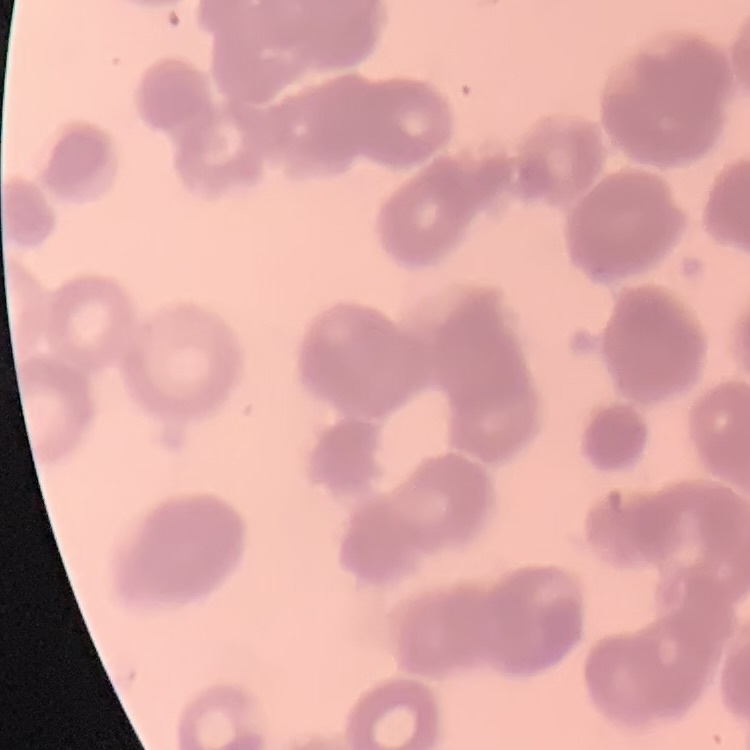

Summary:
  - Erythrocyte morphology: rouleaux formation
  - Stain: Field's or Giemsa
  - Image type: square crop of a larger photomicrograph
  - Preparation: thin blood film